Report the malaria status of this cell.
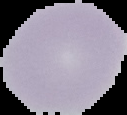

It is uninfected.

Summary:
  - Preparation: thin blood film
  - Image type: segmented cell region on a black background
  - Image size: 127×115 pixels